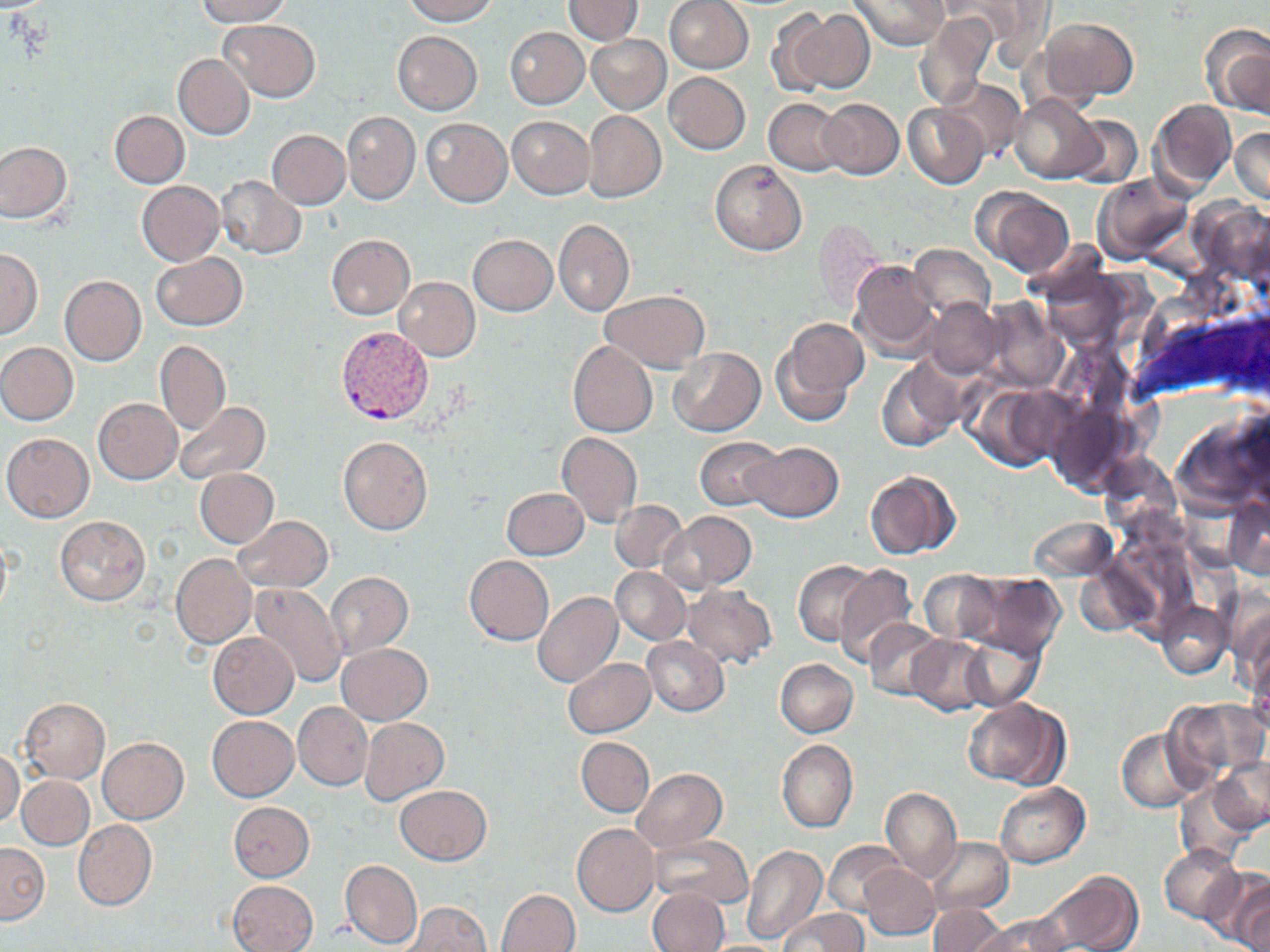
slide-level diagnosis = Plasmodium vivax
magnification = 1000x
stain = May-Grünwald-Giemsa
field of view = one of a larger specimen
modality = light microscopy
Plasmodium vivax-infected red blood cell locations = approximate bounding boxes as named x1/y1/x2/y2 corners in pixels: (x1=336, y1=326, x2=433, y2=425)
preparation = thin blood smear
image size = 1270×952 pixels
uninfected red blood cell locations = approximate bounding boxes as named x1/y1/x2/y2 corners in pixels: (x1=196, y1=0, x2=291, y2=25), (x1=401, y1=0, x2=499, y2=25), (x1=564, y1=0, x2=642, y2=44), (x1=850, y1=0, x2=948, y2=50), (x1=954, y1=0, x2=1054, y2=68), (x1=664, y1=1, x2=753, y2=73), (x1=790, y1=9, x2=875, y2=93), (x1=769, y1=11, x2=835, y2=96), (x1=914, y1=11, x2=999, y2=111), (x1=1038, y1=18, x2=1138, y2=104), (x1=220, y1=20, x2=319, y2=102), (x1=1201, y1=24, x2=1270, y2=117), (x1=505, y1=27, x2=588, y2=108), (x1=392, y1=32, x2=482, y2=114), (x1=586, y1=34, x2=670, y2=115), (x1=173, y1=53, x2=255, y2=140), (x1=664, y1=73, x2=750, y2=154), (x1=938, y1=77, x2=1025, y2=161), (x1=1010, y1=94, x2=1103, y2=183), (x1=819, y1=98, x2=903, y2=179), (x1=1149, y1=98, x2=1236, y2=197), (x1=765, y1=99, x2=848, y2=175), (x1=903, y1=105, x2=990, y2=188), (x1=109, y1=110, x2=189, y2=188), (x1=583, y1=110, x2=666, y2=202), (x1=343, y1=112, x2=419, y2=204), (x1=1067, y1=116, x2=1142, y2=189), (x1=507, y1=117, x2=593, y2=198), (x1=423, y1=119, x2=511, y2=206), (x1=1230, y1=127, x2=1270, y2=205), (x1=266, y1=130, x2=350, y2=209), (x1=0, y1=141, x2=71, y2=223), (x1=710, y1=159, x2=808, y2=256), (x1=216, y1=175, x2=305, y2=258), (x1=1091, y1=175, x2=1192, y2=265), (x1=136, y1=181, x2=225, y2=266), (x1=972, y1=187, x2=1075, y2=279), (x1=1191, y1=197, x2=1270, y2=281), (x1=553, y1=218, x2=634, y2=316), (x1=812, y1=218, x2=888, y2=311), (x1=326, y1=234, x2=415, y2=319), (x1=469, y1=234, x2=557, y2=316), (x1=908, y1=244, x2=997, y2=323), (x1=1, y1=249, x2=41, y2=338), (x1=151, y1=251, x2=247, y2=331), (x1=850, y1=259, x2=940, y2=361), (x1=1037, y1=266, x2=1142, y2=350), (x1=59, y1=276, x2=146, y2=366), (x1=393, y1=278, x2=480, y2=360), (x1=601, y1=290, x2=710, y2=372), (x1=924, y1=298, x2=1004, y2=379), (x1=979, y1=298, x2=1068, y2=393), (x1=776, y1=318, x2=869, y2=419), (x1=155, y1=340, x2=230, y2=435), (x1=567, y1=341, x2=657, y2=436), (x1=0, y1=343, x2=78, y2=425), (x1=668, y1=348, x2=766, y2=436), (x1=877, y1=357, x2=966, y2=451), (x1=968, y1=383, x2=1070, y2=472), (x1=93, y1=398, x2=181, y2=483), (x1=172, y1=401, x2=270, y2=484), (x1=1171, y1=408, x2=1269, y2=518), (x1=2, y1=432, x2=94, y2=521), (x1=557, y1=432, x2=643, y2=528), (x1=338, y1=436, x2=432, y2=535), (x1=695, y1=438, x2=784, y2=511), (x1=743, y1=441, x2=843, y2=523), (x1=1097, y1=452, x2=1182, y2=540), (x1=196, y1=469, x2=279, y2=547), (x1=863, y1=469, x2=962, y2=559), (x1=501, y1=487, x2=588, y2=560), (x1=1223, y1=497, x2=1270, y2=579), (x1=610, y1=500, x2=687, y2=573), (x1=660, y1=511, x2=755, y2=594), (x1=55, y1=515, x2=150, y2=605), (x1=233, y1=516, x2=333, y2=593), (x1=1028, y1=517, x2=1118, y2=582), (x1=170, y1=555, x2=257, y2=648), (x1=464, y1=556, x2=554, y2=644), (x1=793, y1=560, x2=878, y2=645), (x1=1074, y1=560, x2=1162, y2=639), (x1=833, y1=564, x2=919, y2=666), (x1=612, y1=567, x2=690, y2=645), (x1=920, y1=570, x2=1006, y2=647), (x1=953, y1=572, x2=1066, y2=660), (x1=326, y1=573, x2=413, y2=658), (x1=248, y1=583, x2=347, y2=689), (x1=681, y1=584, x2=777, y2=669), (x1=533, y1=591, x2=623, y2=688), (x1=1228, y1=597, x2=1270, y2=697), (x1=1158, y1=601, x2=1231, y2=678), (x1=866, y1=618, x2=948, y2=700), (x1=209, y1=632, x2=298, y2=718), (x1=960, y1=633, x2=1045, y2=710), (x1=643, y1=636, x2=730, y2=716), (x1=909, y1=636, x2=994, y2=715), (x1=338, y1=643, x2=431, y2=724), (x1=1248, y1=649, x2=1270, y2=735), (x1=564, y1=657, x2=655, y2=737), (x1=774, y1=658, x2=858, y2=737), (x1=20, y1=698, x2=110, y2=784), (x1=962, y1=698, x2=1068, y2=789), (x1=1164, y1=698, x2=1268, y2=784), (x1=294, y1=702, x2=372, y2=791), (x1=207, y1=716, x2=299, y2=801), (x1=360, y1=718, x2=449, y2=805), (x1=1117, y1=728, x2=1205, y2=812), (x1=577, y1=737, x2=654, y2=816), (x1=98, y1=738, x2=188, y2=823), (x1=777, y1=740, x2=858, y2=833), (x1=0, y1=749, x2=23, y2=827), (x1=1208, y1=756, x2=1270, y2=836), (x1=630, y1=769, x2=726, y2=853), (x1=18, y1=776, x2=94, y2=849), (x1=1175, y1=778, x2=1258, y2=866), (x1=994, y1=783, x2=1090, y2=867), (x1=394, y1=785, x2=492, y2=864), (x1=880, y1=787, x2=962, y2=883), (x1=229, y1=802, x2=314, y2=881), (x1=73, y1=819, x2=157, y2=911), (x1=573, y1=823, x2=660, y2=916), (x1=649, y1=833, x2=754, y2=910), (x1=925, y1=836, x2=1013, y2=915), (x1=825, y1=840, x2=906, y2=916), (x1=0, y1=842, x2=49, y2=922), (x1=742, y1=845, x2=827, y2=945), (x1=1158, y1=846, x2=1243, y2=923), (x1=341, y1=860, x2=422, y2=948), (x1=859, y1=864, x2=940, y2=940), (x1=1203, y1=869, x2=1270, y2=951), (x1=1036, y1=872, x2=1142, y2=952), (x1=229, y1=880, x2=318, y2=952), (x1=646, y1=888, x2=729, y2=952), (x1=497, y1=889, x2=580, y2=951), (x1=403, y1=901, x2=492, y2=951), (x1=927, y1=903, x2=1008, y2=952), (x1=779, y1=908, x2=868, y2=952), (x1=977, y1=913, x2=1072, y2=952)